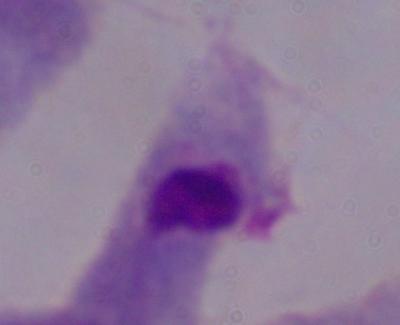
Summary:
  - Modality: micrograph
  - Magnification: 1000x
  - Identification: trichomonad